Assess the morphology of the red blood cells.
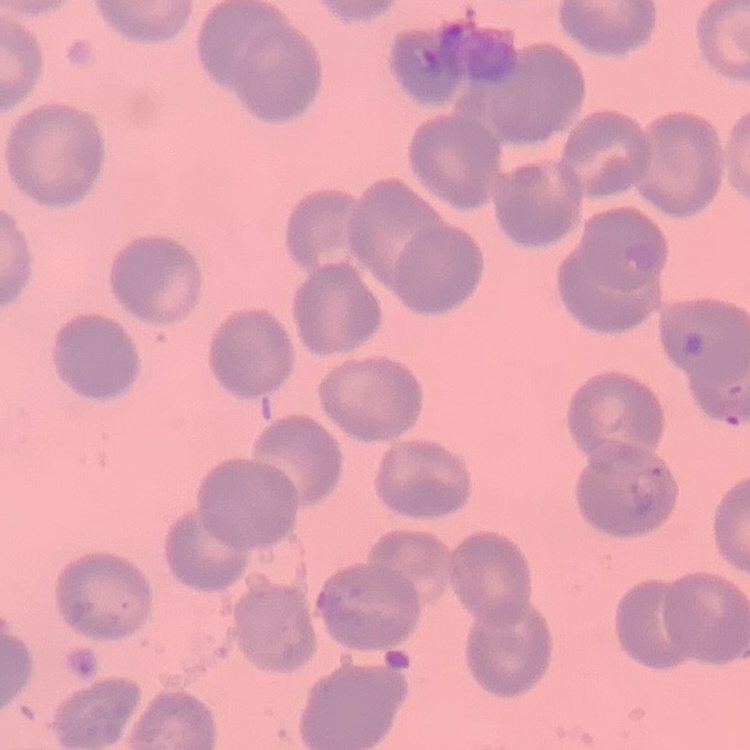
No rouleaux formation.

Summary:
  - Preparation: thin peripheral smear
  - Stain: Field's or Giemsa
  - Image type: one tile cut from a larger photomicrograph